Give the position of every Plasmodium falciparum parasite, noting its life-cycle stage.
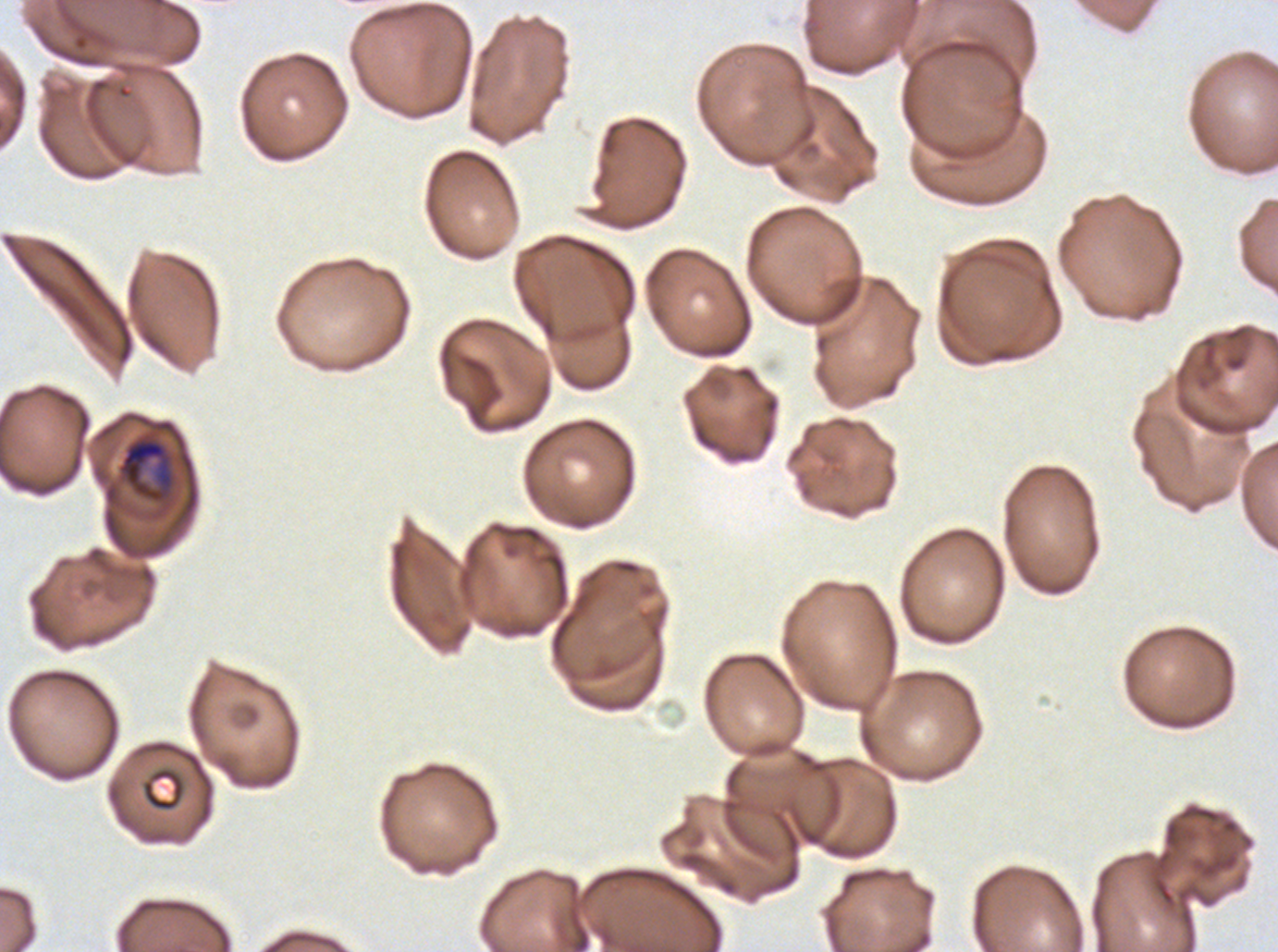

Approximate bounding boxes as [x1, y1, x2, y2] in pixels.
Early schizonts: [117, 435, 175, 504].
No rings, late-ring/early-trophozoite forms, mid trophozoites, late trophozoites, late schizonts, segmenters, or gametocytes observed.

Summary:
  - Debris locations: [141, 767, 186, 812]
  - Image size: 1278×952 pixels
  - Stain: Giemsa
  - Preparation: thin blood film
  - Field of view: one sub-image of a larger composite
  - Specimen: Plasmodium falciparum cultured ex vivo for 24 to 48 hours, from a patient in The Gambia